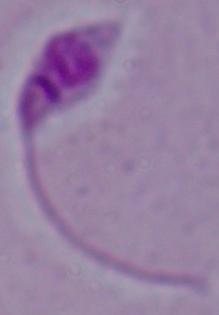
Summary:
  - Modality: micrograph
  - Magnification: 1000x
  - Identification: Leishmania